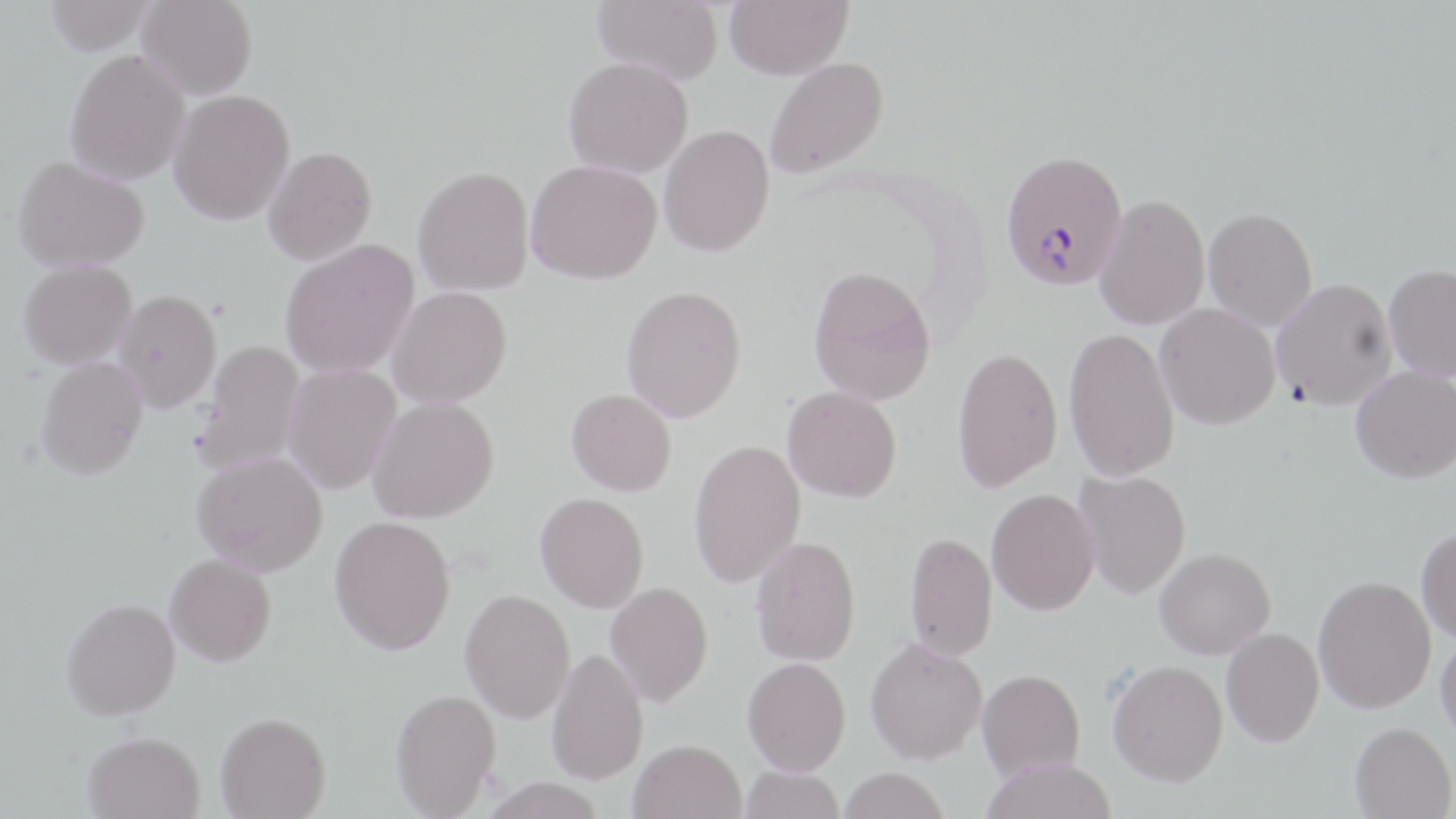 Approximate bounding boxes as (x1, y1, x2, y2) in pixels. Plasmodium falciparum-infected red blood cell locations: (1000, 150, 1127, 291). Uninfected red blood cell locations: (44, 0, 157, 55), (137, 0, 257, 100), (592, 0, 724, 84), (725, 0, 852, 80), (65, 50, 190, 186), (563, 57, 693, 178), (764, 57, 888, 180), (168, 89, 295, 225), (659, 125, 774, 257), (262, 146, 377, 266), (12, 156, 148, 272), (526, 160, 661, 285), (412, 166, 534, 296), (1094, 194, 1210, 331), (1203, 207, 1317, 331), (279, 238, 419, 378), (18, 259, 136, 369), (1383, 264, 1456, 383), (808, 266, 936, 406), (1271, 278, 1397, 409), (387, 285, 512, 408), (621, 285, 747, 422), (114, 289, 221, 413), (1154, 303, 1280, 430), (1063, 327, 1180, 483), (194, 340, 305, 475), (952, 346, 1063, 493), (36, 355, 148, 480), (282, 363, 401, 495), (1351, 365, 1456, 483), (782, 386, 902, 503), (567, 388, 677, 497), (366, 396, 499, 523), (688, 439, 806, 588), (192, 450, 328, 576), (1074, 469, 1191, 598), (986, 489, 1099, 615), (535, 493, 649, 613), (329, 514, 456, 655), (1416, 526, 1456, 644), (904, 532, 998, 662), (750, 536, 861, 666), (1154, 547, 1275, 659), (165, 554, 276, 666), (1313, 575, 1436, 714), (605, 581, 713, 707), (460, 589, 575, 723), (61, 598, 181, 720), (1221, 627, 1324, 748), (1435, 631, 1456, 745), (865, 637, 987, 764), (547, 647, 648, 784), (742, 657, 851, 774), (1107, 659, 1228, 787), (977, 669, 1085, 780), (390, 688, 501, 816), (215, 712, 331, 818), (1350, 722, 1455, 818), (82, 731, 204, 819), (629, 739, 746, 819), (981, 757, 1117, 819), (740, 766, 845, 819), (838, 767, 949, 818), (480, 778, 607, 818). Slide-level diagnosis: Plasmodium falciparum. One field of a larger specimen. Image is 1456×819 pixels. Optical microscopy. May-Grünwald-Giemsa-stained preparation. 1000x magnification. Thin blood smear.